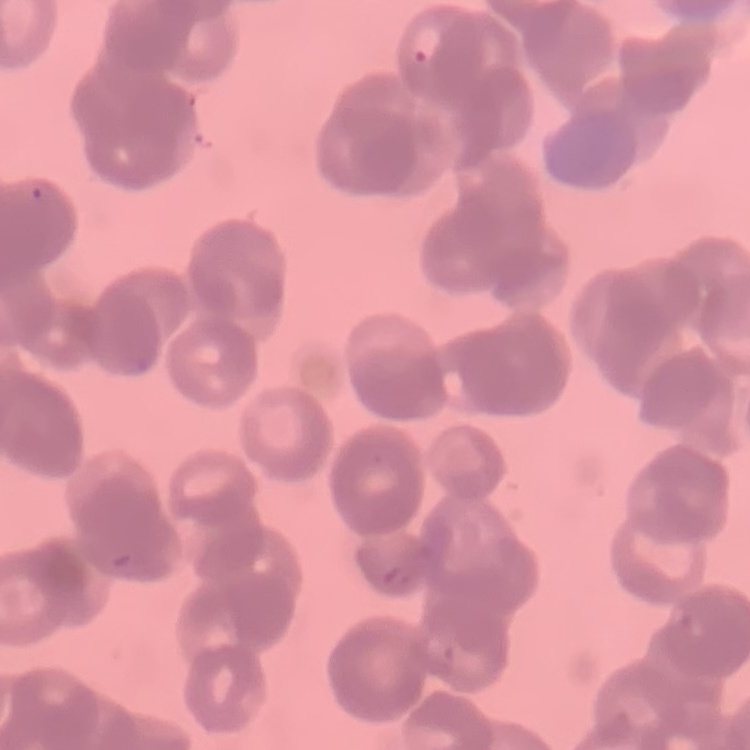 The red blood cells exhibit rouleaux formation. Stained with either Field's or Giemsa. Square crop of a larger photomicrograph. Thin blood film.